Locate and identify every blood parasite.
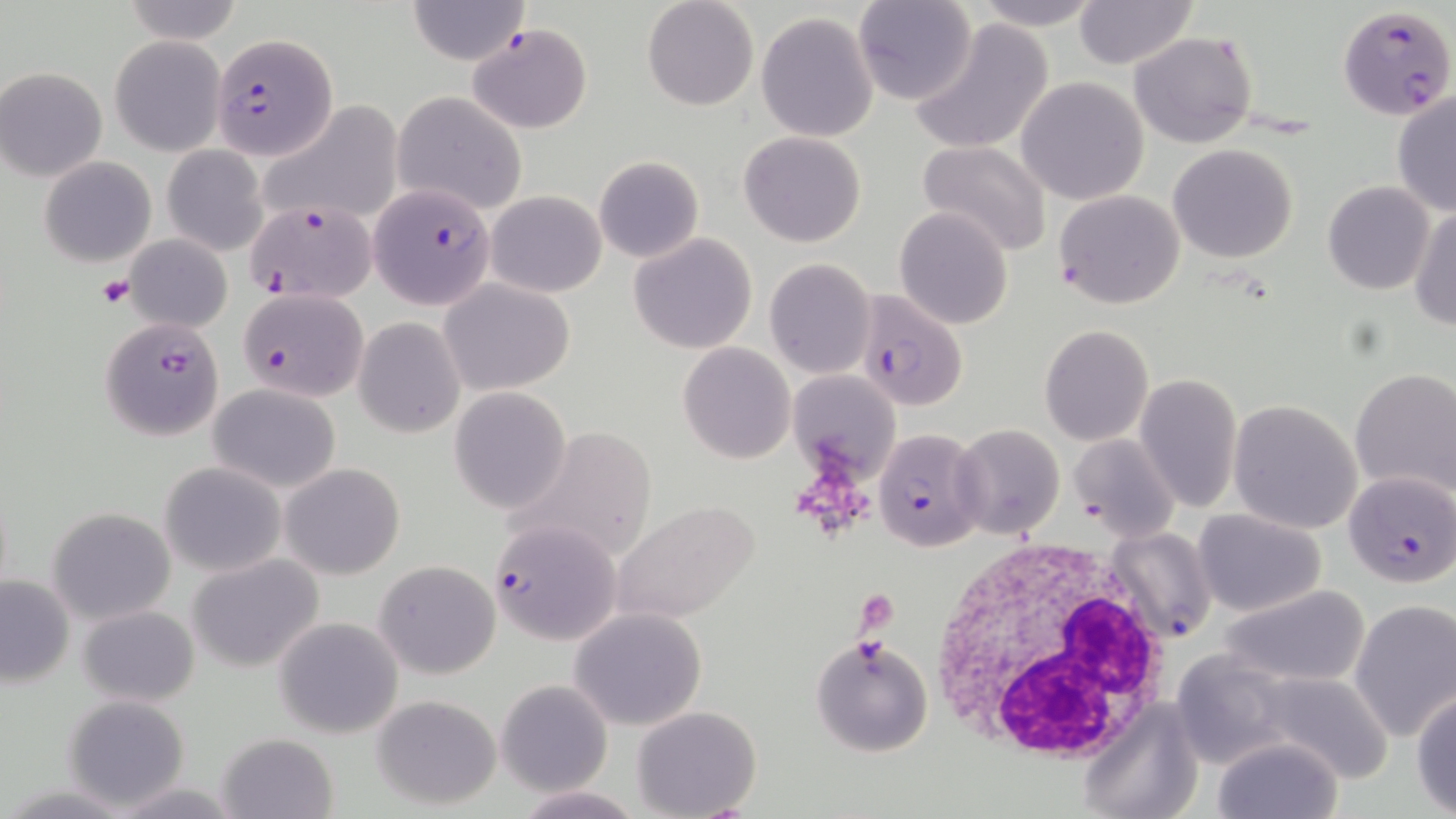

Approximate bounding boxes as [x1, y1, x2, y2] in pixels.
Plasmodium falciparum-infected red blood cells: [1337, 5, 1454, 119], [466, 22, 594, 134], [213, 35, 336, 160], [370, 185, 496, 310], [244, 198, 379, 305], [238, 287, 368, 401], [857, 292, 968, 409], [100, 317, 224, 440], [874, 428, 989, 552], [1341, 469, 1455, 590], [488, 517, 619, 644], [1104, 526, 1216, 643].
No Plasmodium ovale, Plasmodium malariae, Plasmodium vivax, Babesia divergens, or Trypanosoma brucei observed.

Uninfected red blood cell locations: [121, 0, 243, 45], [404, 0, 531, 65], [642, 0, 760, 112], [854, 0, 979, 106], [969, 0, 1107, 30], [1072, 0, 1198, 70], [755, 11, 880, 142], [908, 21, 1054, 155], [1129, 31, 1257, 148], [109, 36, 225, 155], [1, 67, 107, 181], [1015, 76, 1150, 205], [1391, 90, 1456, 217], [393, 91, 528, 217], [260, 101, 403, 225], [739, 130, 867, 247], [916, 141, 1053, 259], [1168, 143, 1299, 263], [162, 145, 269, 256], [39, 156, 157, 266], [594, 156, 703, 263], [1323, 181, 1435, 295], [1053, 189, 1186, 310], [487, 190, 607, 297], [1410, 205, 1456, 331], [895, 209, 1012, 331], [629, 233, 758, 354], [123, 235, 233, 334], [764, 258, 876, 380], [439, 279, 575, 396], [354, 317, 464, 437], [1039, 324, 1153, 447], [678, 342, 795, 463], [787, 368, 902, 486], [1352, 368, 1456, 498], [1135, 372, 1243, 511], [208, 382, 341, 492], [450, 387, 572, 514], [1229, 399, 1363, 533], [953, 424, 1065, 537], [1069, 433, 1178, 540], [160, 461, 287, 576], [281, 462, 405, 579], [609, 500, 763, 625], [47, 506, 176, 625], [1195, 509, 1326, 615], [186, 554, 326, 672], [373, 560, 500, 679], [0, 573, 75, 688], [1218, 584, 1370, 687], [1350, 600, 1456, 742], [78, 605, 200, 707], [570, 610, 707, 732], [273, 617, 404, 738], [810, 635, 935, 758], [1170, 651, 1297, 769], [1259, 671, 1395, 783], [496, 679, 614, 796], [1412, 688, 1456, 814], [62, 694, 191, 810], [370, 694, 503, 811], [1079, 700, 1204, 818], [634, 705, 761, 816], [215, 732, 338, 818], [1212, 735, 1343, 819], [109, 779, 241, 818], [513, 785, 641, 818]. Platelet locations: [98, 275, 135, 309], [855, 589, 898, 636]. White blood cell locations: [926, 538, 1179, 768]. Slide-level diagnosis: Plasmodium falciparum. Captured at 1000x magnification. Single field of view. Image is 1456×819 pixels. Light microscopy. Thin blood film. May-Grünwald-Giemsa-stained preparation.